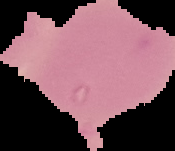
Summary:
  - Image type: cell region segmented out of the field of view; surrounding area masked to black
  - Preparation: thin blood film
  - Image size: 175×151 pixels
  - Result: negative for malaria parasites